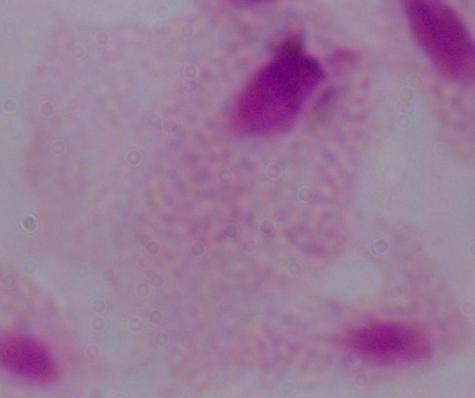

Summary:
  - Magnification: 1000x
  - Modality: photomicrograph
  - Identification: trichomonad